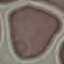

Summary:
  - Result: no malaria parasites detected
  - Image type: cell patch, automatically extracted from a larger field of view and resized to 64 × 64 pixels
  - Preparation: thin blood smear
  - Stain: Giemsa
  - Capture: smartphone camera at the microscope eyepiece